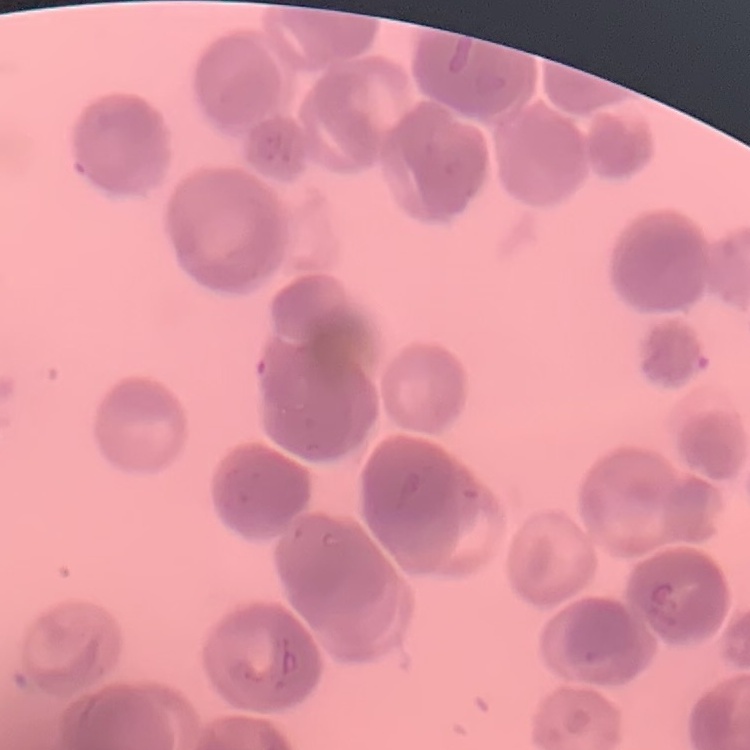

Summary:
  - Erythrocyte morphology: rouleaux formation
  - Stain: Field's or Giemsa
  - Preparation: thin peripheral smear
  - Image type: one tile cut from a larger photomicrograph